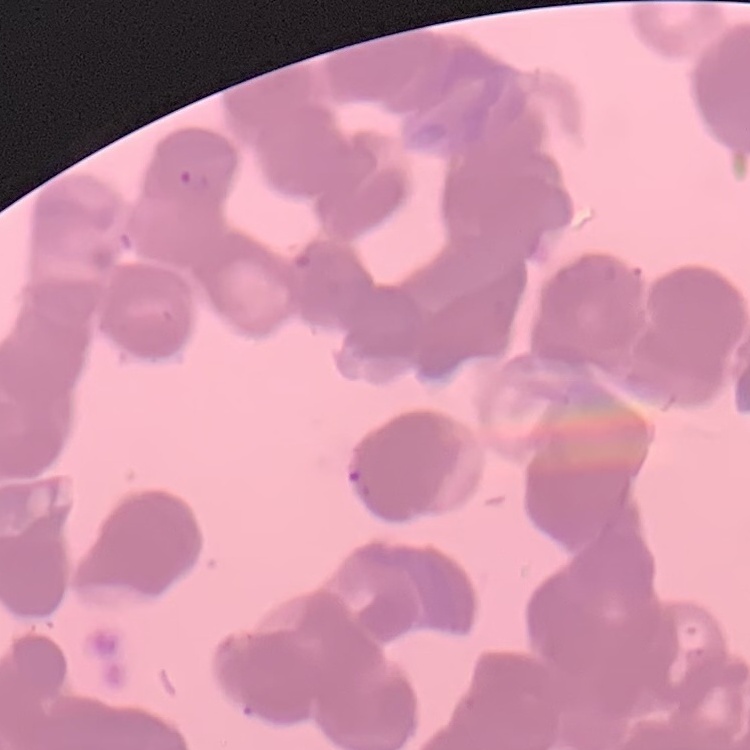
Summary:
  - Erythrocyte morphology: rouleaux formation
  - Preparation: thin blood film
  - Stain: Field's or Giemsa
  - Image type: square crop of a larger photomicrograph